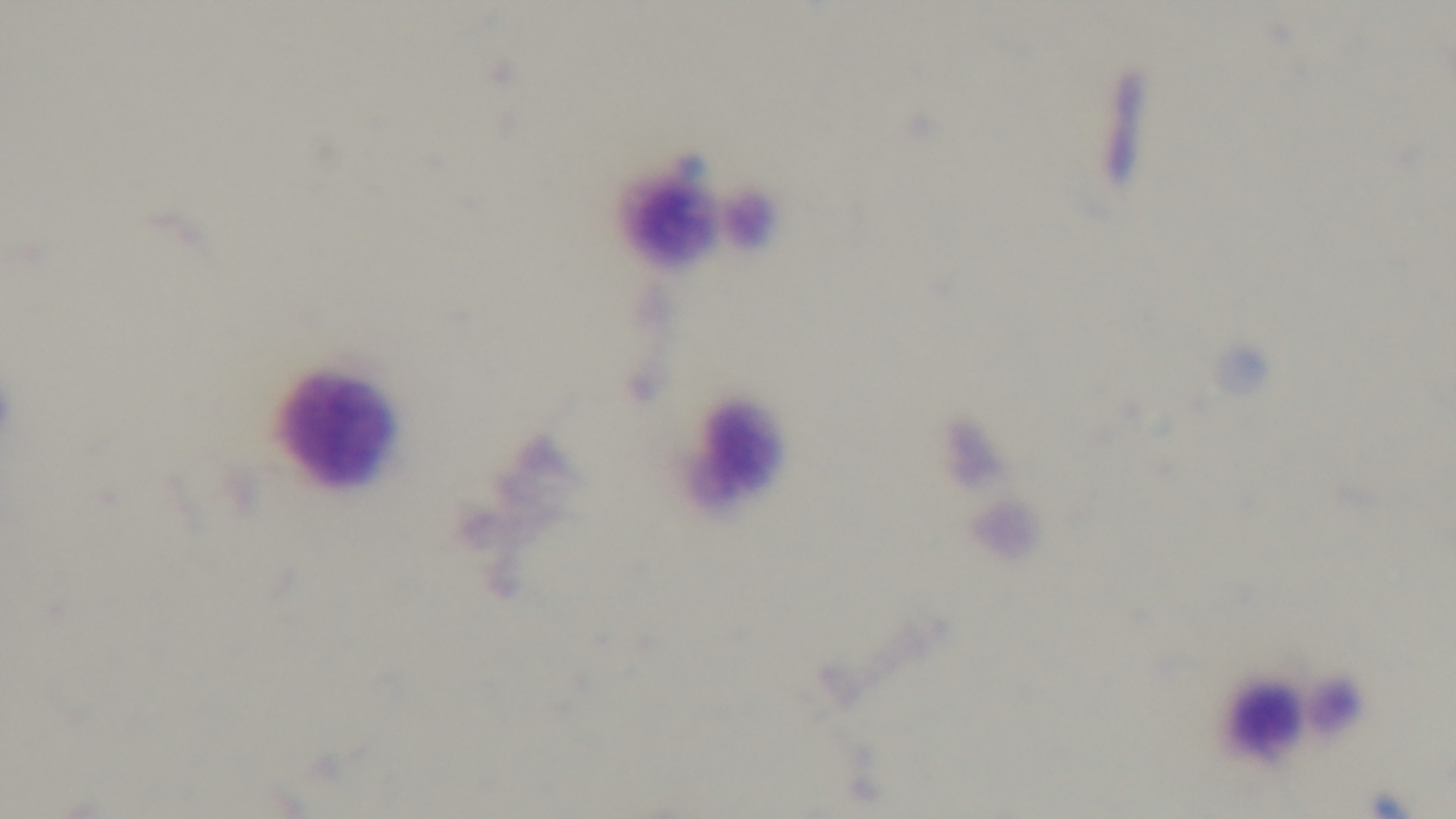
objective: 100x oil immersion
stain: Giemsa
modality: light microscopy
preparation: thick blood film
capture: mounted 4K digital camera
field_of_view: one from the slide
malaria_status: negative